Classify this cell by malaria status.
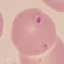

It is parasitized.

Photographed with a smartphone camera at the microscope eyepiece. Thin smear of blood. Cell patch, automatically extracted from a larger field of view and resized to 64 × 64 pixels. Giemsa stain.